Classify this cell by malaria status.
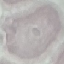
It is uninfected.

preparation = thin blood film
stain = Giemsa
capture = smartphone camera at the microscope eyepiece
image type = automatically extracted cell patch, resized to 64 × 64 pixels